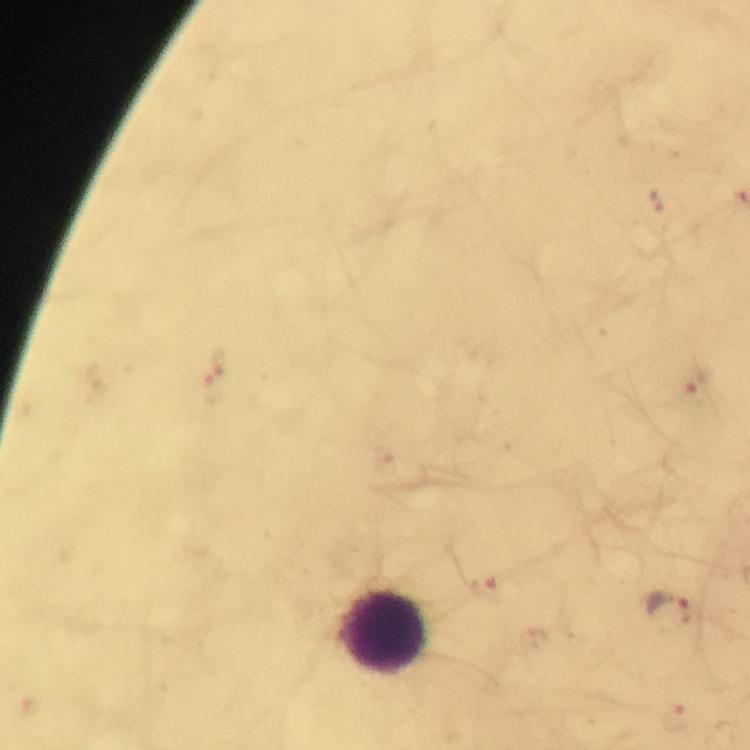
Approximate centers as [x, y] in pixels. Leukocyte locations: [384, 633]. Plasmodium parasite locations: [656, 200], [221, 362], [695, 383], [214, 390], [483, 590], [672, 610], [676, 718]. Photographed through the microscope with a smartphone camera. From a diagnostic examination for malaria. Immersion oil was used. Image is 750×750 pixels. Giemsa stain. Cropped region of a single field of view. 100x magnification. Thick blood smear.